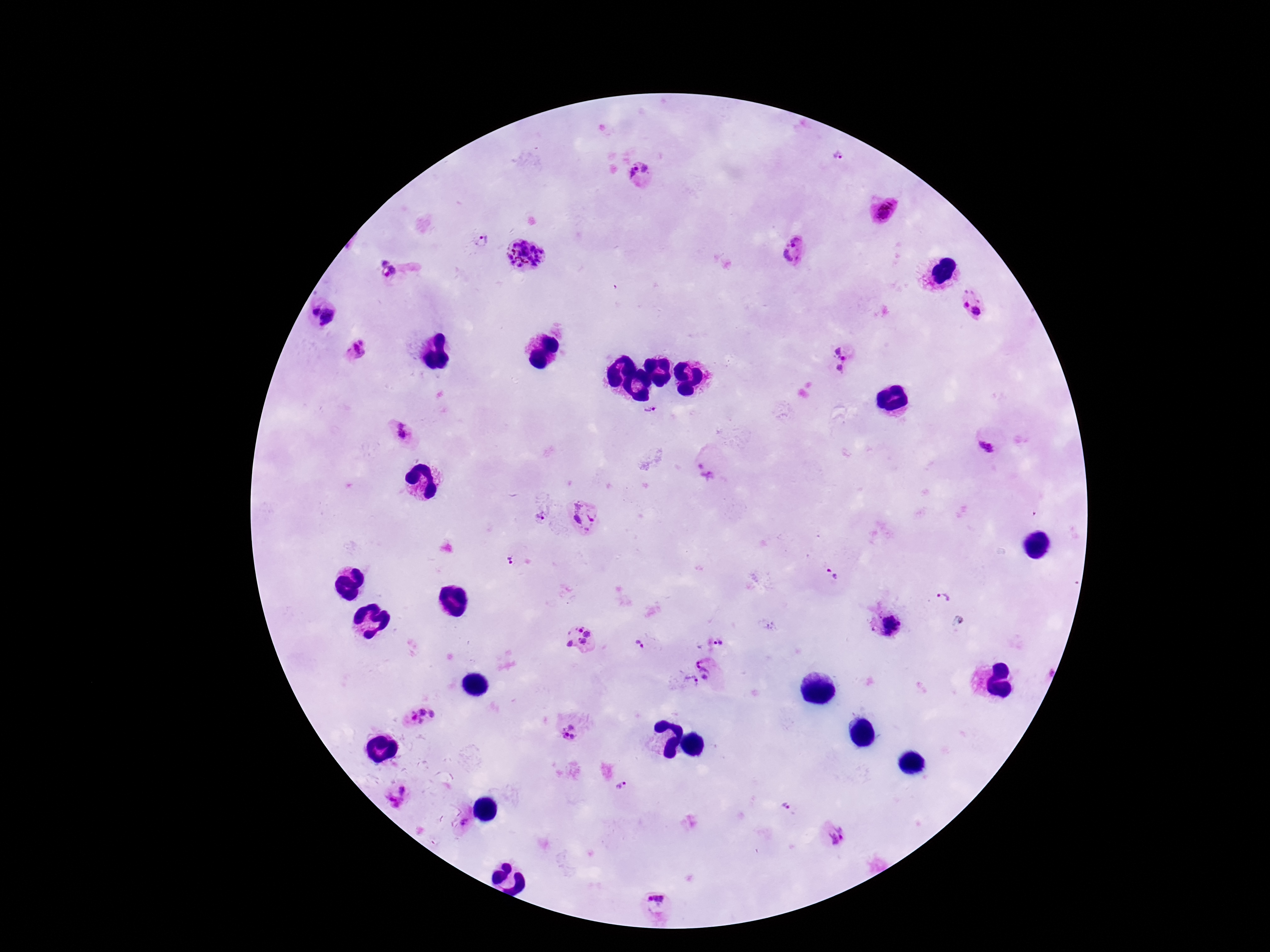
Approximate centers as {x, y} in pixels.
Summary:
  - Plasmodium parasite locations: {838, 156}, {638, 171}, {882, 210}, {482, 242}, {793, 251}, {523, 253}, {384, 261}, {390, 274}, {972, 300}, {315, 312}, {330, 318}, {356, 350}, {837, 351}, {844, 359}, {838, 369}, {653, 414}, {399, 430}, {990, 449}, {706, 469}, {541, 517}, {585, 518}, {509, 561}, {832, 573}, {942, 598}, {891, 626}, {580, 638}, {718, 642}, {639, 644}, {706, 667}, {690, 682}, {419, 717}, {569, 733}, {622, 786}, {403, 791}, {394, 802}, {784, 805}, {466, 822}, {836, 835}, {656, 900}
  - Magnification: 100x
  - Capture: smartphone camera through the microscope eyepiece
  - Preparation: thick blood smear
  - Patient malaria status: infected
  - Stain: Giemsa
  - Image size: 1270×952 pixels
  - Field of view: single